State which cell type is depicted.
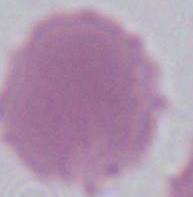

This is an erythrocyte.

magnification = 1000x
modality = photomicrograph